Name the cell type shown.
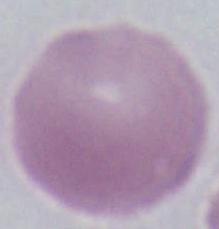

An erythrocyte.

1000x magnification. Micrograph.